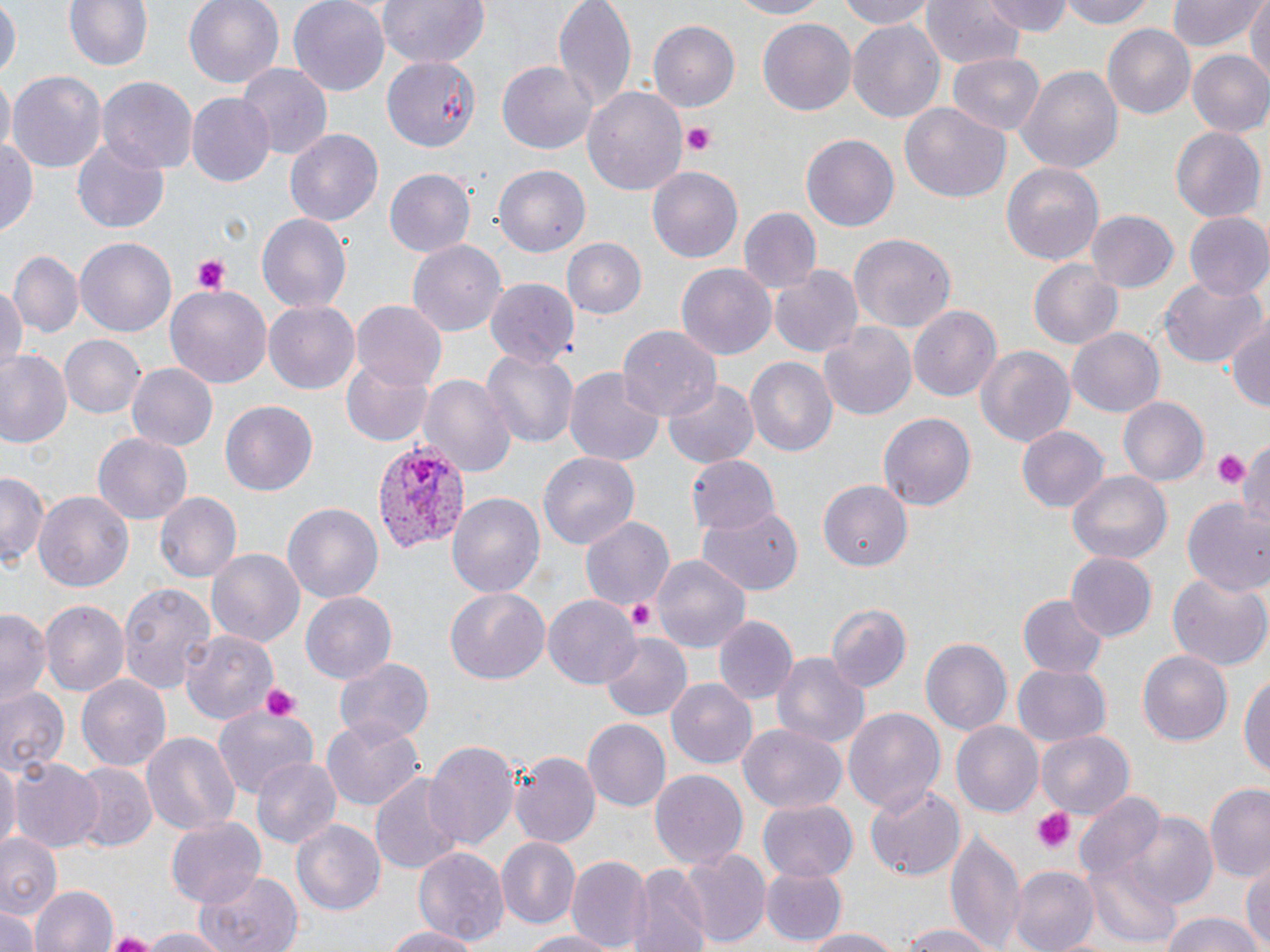

Approximate bounding boxes as [x1, y1, x2, y2] in pixels. Uninfected red blood cell locations: [62, 0, 154, 71], [184, 0, 283, 89], [288, 0, 390, 94], [379, 0, 490, 68], [552, 0, 636, 110], [722, 0, 832, 19], [832, 0, 938, 29], [984, 0, 1072, 36], [1054, 0, 1162, 29], [1168, 0, 1262, 52], [1247, 0, 1270, 89], [0, 1, 18, 83], [921, 1, 1025, 68], [847, 18, 947, 126], [757, 19, 856, 116], [648, 21, 739, 111], [1103, 24, 1195, 119], [381, 48, 480, 153], [1186, 49, 1270, 137], [947, 52, 1045, 133], [237, 63, 332, 161], [498, 63, 595, 154], [1016, 64, 1124, 173], [7, 68, 106, 174], [0, 77, 14, 153], [98, 77, 198, 173], [582, 85, 688, 196], [186, 93, 276, 186], [900, 102, 1010, 205], [1170, 127, 1264, 222], [285, 129, 384, 227], [0, 134, 38, 238], [801, 134, 899, 231], [73, 139, 169, 235], [1001, 160, 1105, 266], [493, 164, 591, 256], [646, 166, 744, 264], [386, 168, 476, 259], [739, 208, 821, 292], [1086, 209, 1180, 290], [257, 212, 351, 317], [1183, 213, 1270, 303], [849, 233, 956, 332], [74, 235, 177, 338], [560, 237, 646, 321], [409, 239, 507, 337], [9, 250, 81, 338], [1029, 261, 1122, 349], [675, 262, 776, 360], [770, 265, 863, 361], [1161, 277, 1265, 368], [0, 278, 25, 380], [486, 278, 580, 369], [165, 281, 273, 387], [263, 299, 359, 391], [353, 301, 447, 392], [911, 306, 1002, 404], [1225, 312, 1270, 410], [818, 320, 918, 420], [617, 327, 721, 422], [1068, 327, 1165, 417], [59, 334, 146, 419], [974, 342, 1076, 447], [0, 349, 71, 448], [482, 349, 578, 449], [343, 356, 436, 446], [743, 356, 837, 459], [126, 362, 216, 451], [563, 365, 665, 467], [420, 373, 516, 480], [663, 378, 759, 468], [1119, 395, 1208, 487], [220, 401, 317, 497], [878, 409, 976, 509], [1016, 425, 1108, 514], [93, 433, 191, 523], [1235, 433, 1270, 532], [539, 452, 639, 550], [686, 456, 779, 538], [1, 472, 47, 569], [1066, 472, 1171, 567], [818, 479, 914, 569], [35, 491, 134, 591], [153, 491, 241, 584], [448, 491, 545, 599], [1184, 499, 1270, 600], [283, 504, 382, 602], [698, 508, 803, 596], [579, 514, 673, 612], [207, 547, 304, 649], [1065, 551, 1156, 641], [652, 554, 753, 650], [1168, 569, 1270, 670], [120, 579, 216, 692], [445, 589, 550, 684], [300, 591, 398, 685], [1019, 595, 1109, 679], [545, 596, 640, 688], [41, 599, 130, 697], [824, 604, 911, 693], [0, 610, 50, 708], [713, 614, 797, 707], [181, 627, 279, 723], [600, 634, 690, 718], [921, 638, 1013, 737], [1138, 649, 1231, 746], [771, 651, 870, 750], [333, 654, 436, 746], [1013, 666, 1111, 747], [1239, 670, 1269, 783], [75, 672, 171, 773], [666, 679, 756, 768], [0, 684, 69, 777], [843, 706, 945, 815], [211, 707, 318, 796], [322, 718, 423, 811], [581, 720, 671, 813], [738, 722, 848, 814], [951, 722, 1043, 817], [141, 730, 240, 836], [1036, 731, 1135, 819], [423, 738, 518, 851], [510, 750, 600, 849], [0, 756, 18, 856], [251, 756, 340, 850], [9, 758, 105, 852], [68, 763, 156, 853], [648, 769, 747, 870], [367, 770, 466, 878], [1205, 783, 1270, 883], [866, 784, 966, 878], [1075, 793, 1170, 886], [757, 801, 856, 882], [1115, 812, 1218, 908], [166, 816, 267, 908], [291, 819, 386, 919], [947, 828, 1025, 951], [0, 831, 63, 918], [497, 837, 580, 928], [412, 846, 507, 948], [679, 848, 769, 948], [569, 853, 651, 951], [1242, 859, 1270, 949], [1088, 861, 1179, 948], [759, 865, 847, 947], [628, 866, 709, 952], [1009, 866, 1098, 952], [195, 871, 302, 952], [31, 885, 118, 952], [0, 905, 41, 952], [1157, 911, 1263, 952], [893, 923, 1003, 952], [381, 925, 482, 952], [133, 927, 232, 952], [795, 927, 909, 952], [522, 929, 624, 952]. Plasmodium vivax-infected red blood cell locations: [370, 440, 470, 555]. Platelet locations: [684, 122, 716, 156], [192, 254, 230, 295], [1213, 449, 1248, 491], [626, 599, 656, 630], [259, 684, 300, 724], [1032, 808, 1072, 852]. Slide-level diagnosis: Plasmodium vivax. May-Grünwald-Giemsa-stained preparation. One field of a larger specimen. Optical microscopy. Thin blood film. Image is 1270×952 pixels. 1000x magnification.